Outline each blood parasite and name the species.
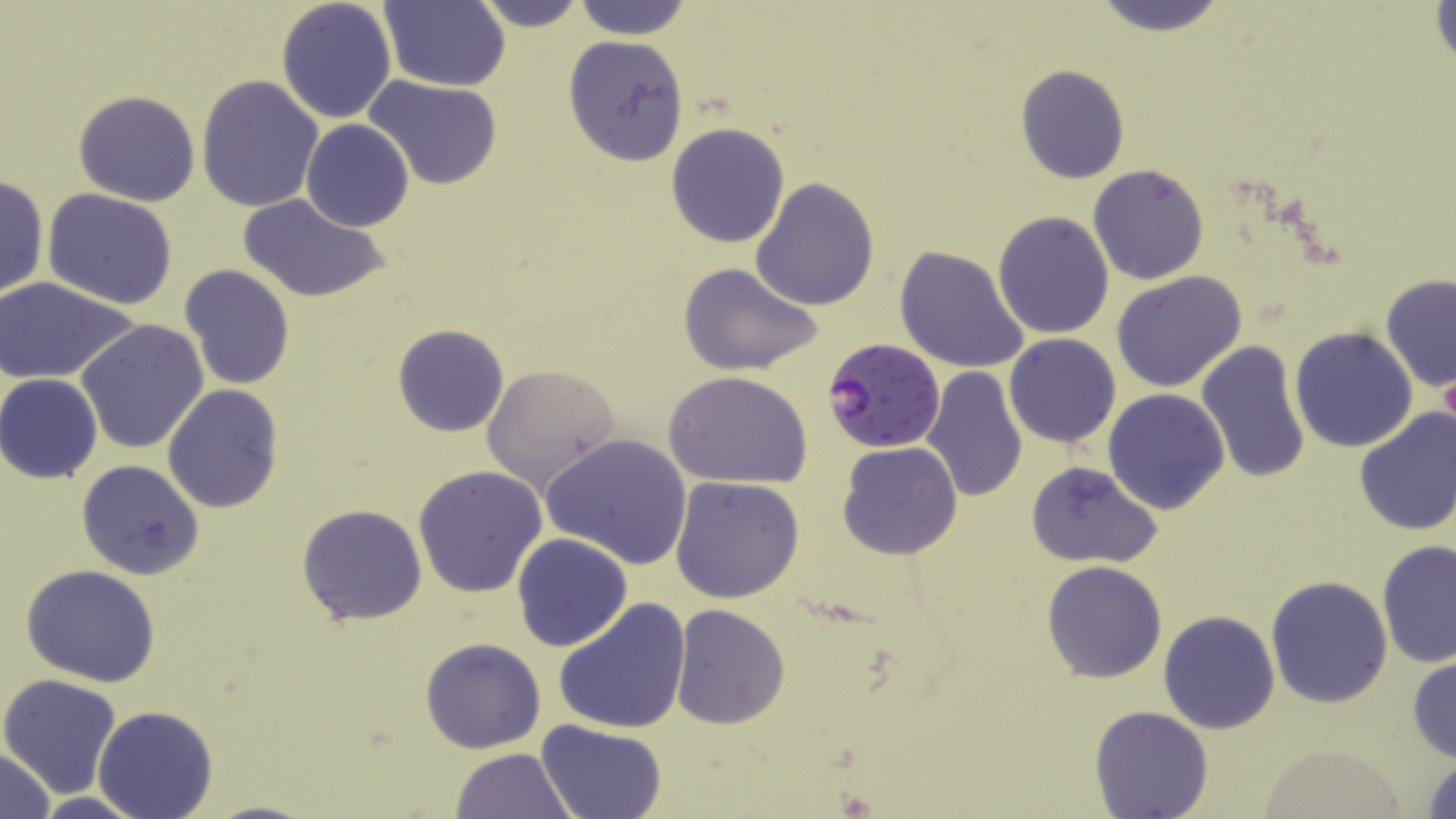
Approximate bounding boxes as named x1/y1/x2/y2 corners in pixels.
Plasmodium falciparum-infected red blood cells: (x1=822, y1=339, x2=945, y2=453).
No Plasmodium ovale, Plasmodium malariae, Plasmodium vivax, Babesia divergens, or Trypanosoma brucei observed.

Uninfected red blood cell locations: (x1=275, y1=0, x2=397, y2=122), (x1=381, y1=0, x2=511, y2=91), (x1=474, y1=0, x2=587, y2=32), (x1=571, y1=0, x2=694, y2=40), (x1=1086, y1=0, x2=1234, y2=34), (x1=1429, y1=1, x2=1455, y2=74), (x1=563, y1=36, x2=691, y2=164), (x1=1014, y1=64, x2=1129, y2=184), (x1=196, y1=74, x2=324, y2=214), (x1=363, y1=74, x2=504, y2=190), (x1=72, y1=90, x2=201, y2=207), (x1=301, y1=120, x2=415, y2=232), (x1=665, y1=122, x2=791, y2=249), (x1=1087, y1=165, x2=1209, y2=285), (x1=0, y1=177, x2=49, y2=299), (x1=750, y1=178, x2=880, y2=309), (x1=43, y1=189, x2=178, y2=309), (x1=239, y1=195, x2=390, y2=303), (x1=991, y1=210, x2=1115, y2=339), (x1=894, y1=245, x2=1031, y2=374), (x1=677, y1=262, x2=824, y2=377), (x1=179, y1=265, x2=297, y2=391), (x1=1112, y1=272, x2=1247, y2=393), (x1=1380, y1=272, x2=1456, y2=393), (x1=0, y1=276, x2=141, y2=384), (x1=74, y1=319, x2=209, y2=455), (x1=392, y1=324, x2=508, y2=437), (x1=1289, y1=326, x2=1418, y2=451), (x1=1004, y1=333, x2=1121, y2=447), (x1=1196, y1=340, x2=1311, y2=484), (x1=480, y1=364, x2=621, y2=492), (x1=918, y1=366, x2=1030, y2=503), (x1=664, y1=370, x2=813, y2=491), (x1=1, y1=374, x2=103, y2=484), (x1=162, y1=384, x2=284, y2=514), (x1=1103, y1=388, x2=1231, y2=514), (x1=1352, y1=407, x2=1456, y2=537), (x1=541, y1=434, x2=693, y2=569), (x1=837, y1=441, x2=963, y2=561), (x1=76, y1=458, x2=205, y2=580), (x1=1025, y1=460, x2=1165, y2=568), (x1=413, y1=465, x2=548, y2=597), (x1=671, y1=478, x2=805, y2=605), (x1=296, y1=503, x2=428, y2=626), (x1=512, y1=533, x2=633, y2=653), (x1=1377, y1=540, x2=1456, y2=670), (x1=1042, y1=561, x2=1167, y2=682), (x1=20, y1=564, x2=162, y2=686), (x1=1265, y1=574, x2=1394, y2=707), (x1=554, y1=597, x2=692, y2=735), (x1=671, y1=603, x2=791, y2=730), (x1=1158, y1=609, x2=1282, y2=734), (x1=420, y1=637, x2=546, y2=754), (x1=1407, y1=653, x2=1456, y2=764), (x1=1, y1=673, x2=123, y2=799), (x1=93, y1=703, x2=218, y2=819), (x1=1089, y1=706, x2=1214, y2=819), (x1=537, y1=719, x2=667, y2=819), (x1=1252, y1=743, x2=1412, y2=817), (x1=0, y1=746, x2=56, y2=819), (x1=448, y1=747, x2=578, y2=819), (x1=1421, y1=753, x2=1456, y2=817), (x1=30, y1=793, x2=144, y2=819), (x1=203, y1=799, x2=326, y2=819). Slide-level diagnosis: Plasmodium falciparum. Single field of view. May-Grünwald-Giemsa-stained preparation. Image is 1456×819 pixels. Optical microscopy. Thin blood smear. 1000x magnification.